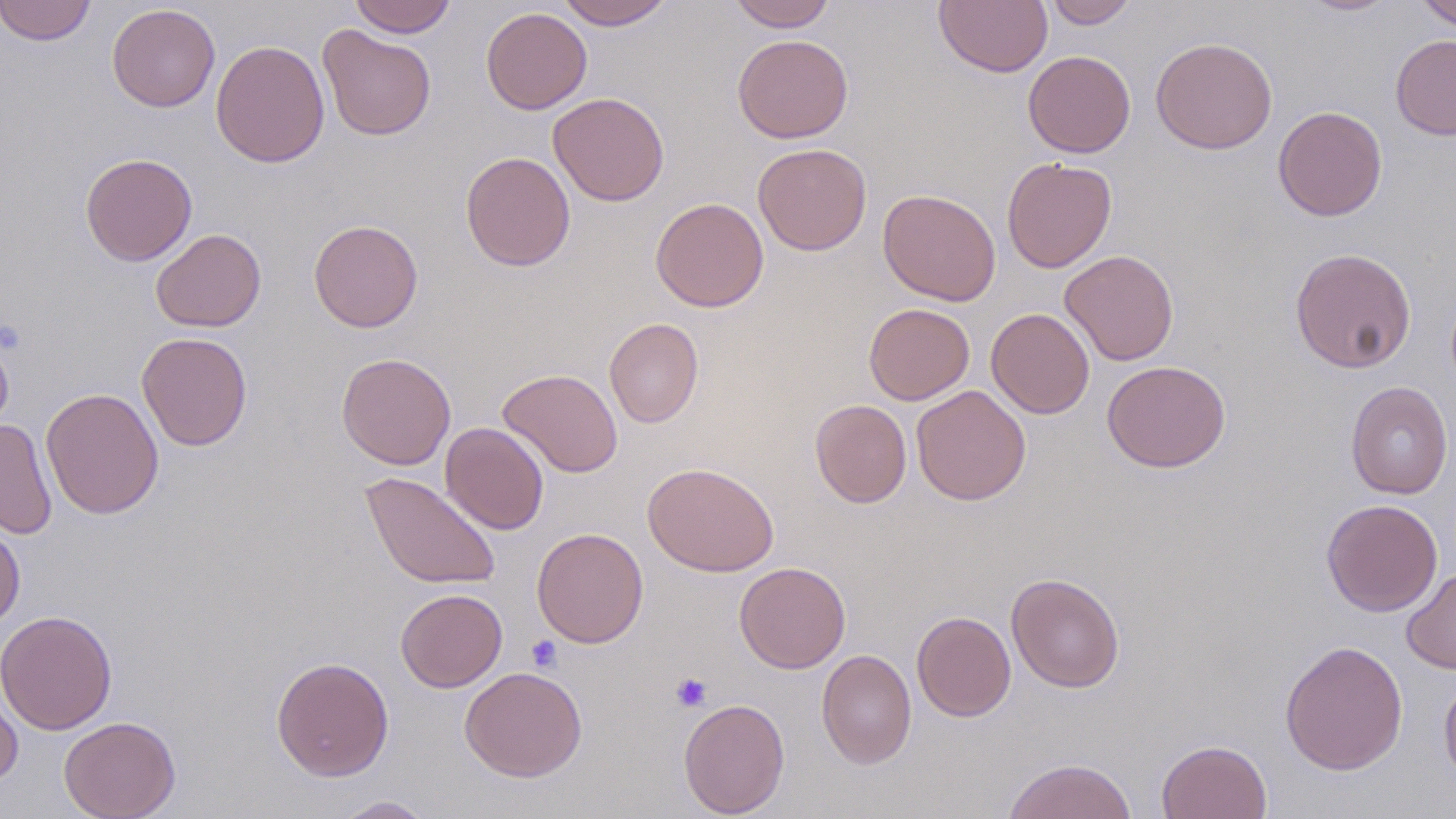

Approximate bounding boxes as [x1, y1, x2, y2] in pixels. Uninfected red blood cell locations: [0, 0, 96, 45], [348, 0, 457, 38], [556, 0, 675, 30], [728, 0, 837, 32], [934, 0, 1053, 76], [1044, 0, 1138, 28], [1417, 0, 1456, 32], [1299, 1, 1398, 16], [107, 3, 220, 112], [481, 7, 592, 114], [317, 24, 436, 141], [731, 34, 854, 143], [1390, 34, 1456, 140], [1150, 36, 1278, 154], [210, 39, 330, 167], [1023, 50, 1135, 158], [548, 92, 670, 207], [1272, 105, 1388, 221], [753, 143, 872, 255], [460, 151, 576, 271], [80, 152, 198, 266], [1001, 157, 1117, 273], [878, 189, 1001, 306], [650, 196, 769, 312], [308, 219, 423, 333], [151, 228, 266, 332], [1289, 247, 1417, 373], [1060, 249, 1178, 366], [864, 303, 975, 405], [986, 308, 1095, 418], [604, 318, 704, 427], [0, 327, 14, 437], [136, 332, 252, 451], [336, 352, 456, 470], [1102, 359, 1231, 473], [497, 368, 624, 477], [1346, 381, 1453, 499], [911, 385, 1031, 505], [41, 387, 164, 519], [810, 399, 912, 508], [0, 418, 57, 539], [440, 422, 550, 534], [643, 461, 779, 576], [361, 471, 502, 590], [1321, 498, 1443, 616], [0, 520, 25, 632], [532, 527, 649, 648], [734, 562, 850, 673], [1401, 567, 1456, 674], [1006, 572, 1125, 693], [395, 588, 508, 692], [0, 610, 118, 736], [911, 611, 1016, 721], [1279, 639, 1408, 775], [816, 649, 917, 769], [271, 656, 394, 781], [460, 666, 587, 782], [1439, 674, 1456, 789], [0, 677, 23, 791], [678, 697, 790, 817], [58, 715, 181, 819], [1156, 739, 1272, 819], [1003, 757, 1139, 819], [330, 795, 436, 818]. Platelet locations: [527, 635, 563, 672], [670, 672, 712, 713]. Slide-level diagnosis: negative for blood parasites. Captured at 1000x magnification. Optical microscopy. May-Grünwald-Giemsa stain. Thin blood smear. One field of a larger specimen. Image is 1456×819 pixels.